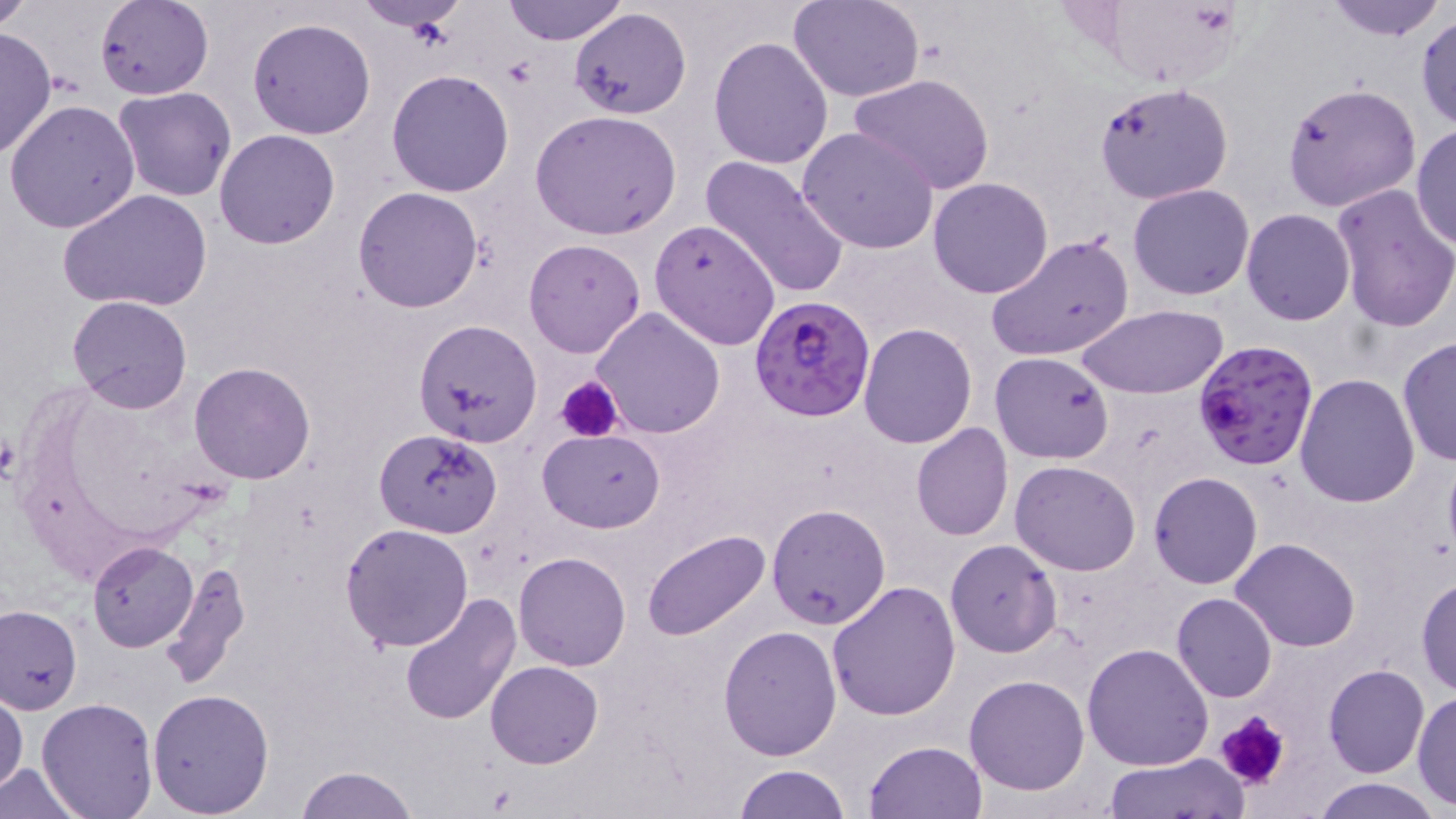

Approximate bounding boxes as (x1,y1)-(x2,y2) corner pairs in pixels. Platelet locations: (500,58)-(540,89), (556,376)-(622,442), (1,433)-(19,479), (1214,710)-(1293,792). Plasmodium falciparum-infected red blood cell locations: (751,296)-(876,423), (1193,336)-(1322,470). Uninfected red blood cell locations: (0,0)-(35,30), (353,0)-(473,31), (500,0)-(630,45), (790,0)-(925,102), (1100,0)-(1244,89), (1322,0)-(1446,40), (95,1)-(215,100), (568,8)-(691,119), (1416,13)-(1456,133), (247,16)-(377,140), (0,27)-(56,158), (709,37)-(834,171), (386,69)-(514,196), (848,73)-(995,194), (1094,81)-(1232,205), (1283,82)-(1420,211), (113,85)-(236,201), (4,99)-(141,234), (529,110)-(682,239), (1410,122)-(1456,252), (796,126)-(939,254), (214,129)-(340,249), (699,156)-(849,300), (928,178)-(1054,298), (1128,183)-(1255,300), (1330,183)-(1456,333), (353,186)-(484,313), (60,190)-(212,315), (1241,208)-(1355,327), (649,218)-(782,350), (986,233)-(1135,362), (523,238)-(646,357), (67,294)-(194,414), (1077,303)-(1228,400), (590,306)-(725,439), (414,320)-(542,446), (857,323)-(977,448), (1397,337)-(1455,467), (990,351)-(1114,463), (188,362)-(316,484), (1294,373)-(1421,507), (910,422)-(1013,541), (373,427)-(502,538), (537,429)-(666,532), (1010,460)-(1141,575), (1148,472)-(1263,589), (766,503)-(891,630), (340,522)-(474,650), (642,529)-(769,642), (1231,537)-(1360,652), (945,539)-(1063,658), (87,541)-(197,651), (514,551)-(632,671), (162,559)-(251,689), (1415,573)-(1456,696), (828,580)-(961,722), (1170,592)-(1277,704), (398,594)-(522,725), (0,606)-(82,714), (717,625)-(841,761), (1083,641)-(1215,771), (484,661)-(603,768), (1324,664)-(1430,779), (964,673)-(1091,794), (147,686)-(276,815), (0,689)-(27,796), (1414,689)-(1455,811), (35,698)-(160,819), (864,740)-(986,819), (1101,754)-(1248,818), (0,760)-(88,818), (732,764)-(851,819), (292,766)-(419,819), (1309,777)-(1446,819). Slide-level diagnosis: Plasmodium falciparum. Single field of view. 1000x magnification. Image is 1456×819 pixels. Thin blood film. Light microscopy. May-Grünwald-Giemsa stain.